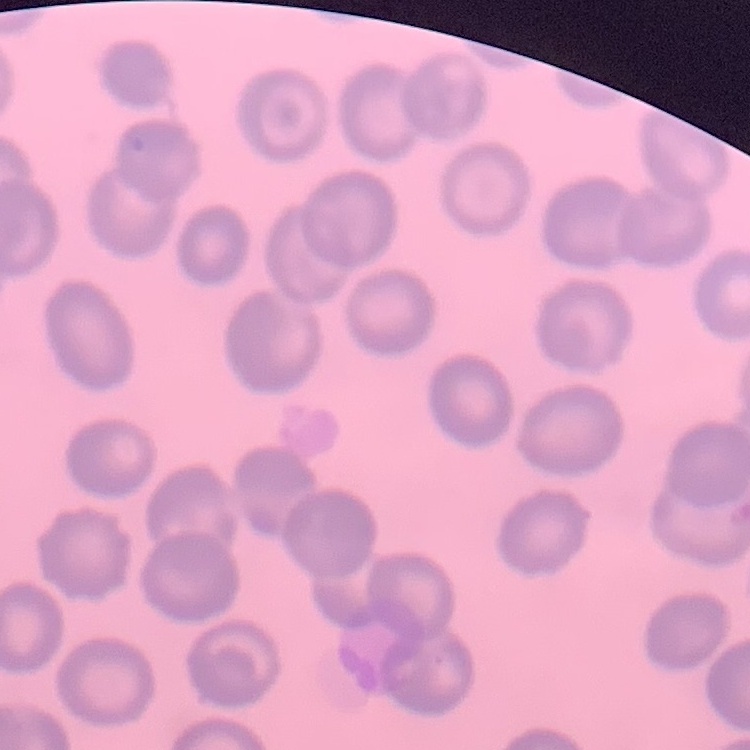

Summary:
  - Red blood cell morphology: no rouleaux formation
  - Stain: Field's or Giemsa
  - Image type: square crop of a larger photomicrograph
  - Preparation: thin peripheral smear